Point out each Plasmodium parasite.
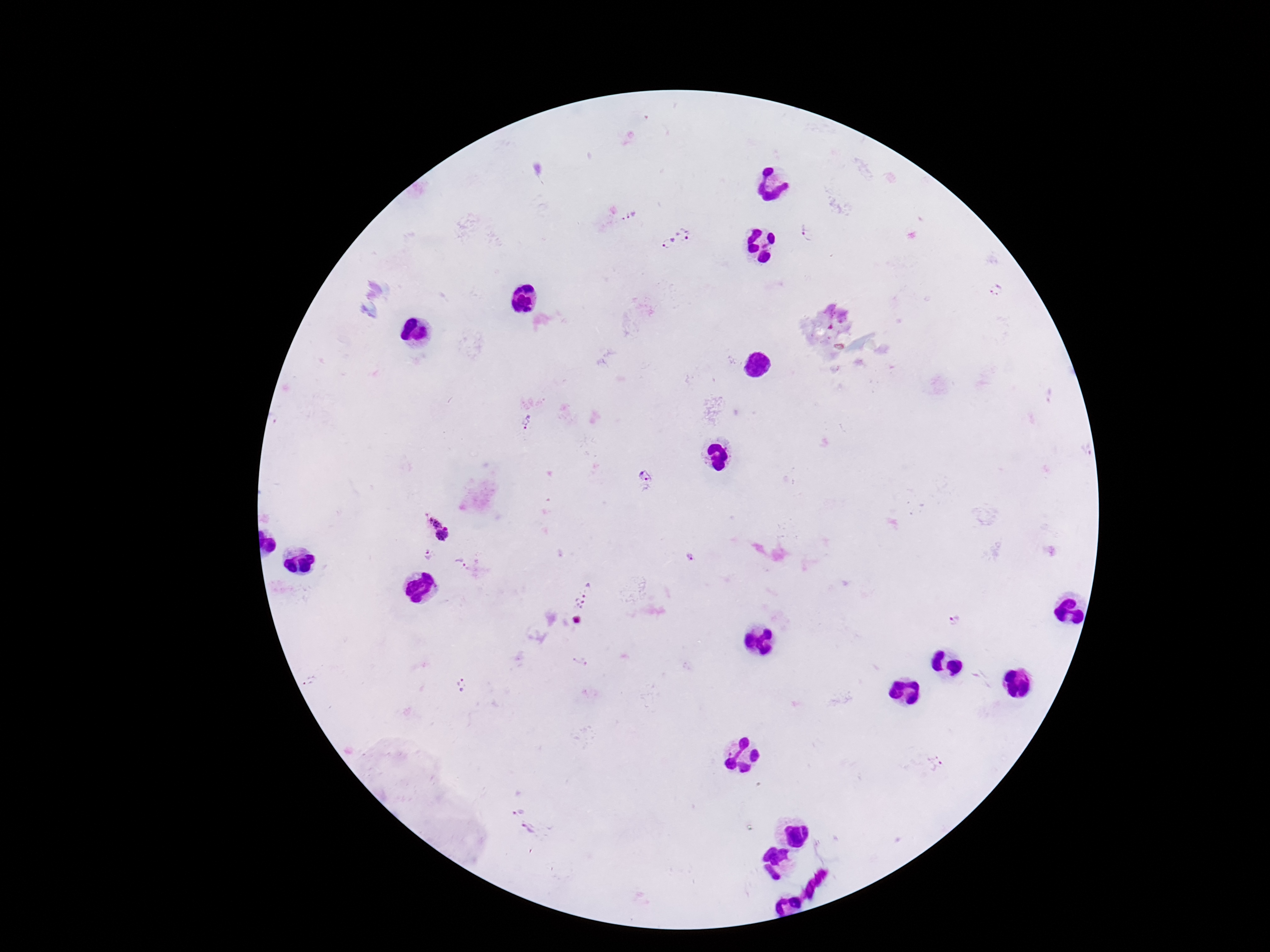
Approximate centers as {x, y} in pixels.
Plasmodium parasites: {632, 217}, {687, 229}, {807, 234}, {668, 243}, {996, 290}, {528, 422}, {646, 473}, {438, 526}, {428, 553}, {461, 562}, {585, 595}, {953, 620}, {935, 762}, {517, 808}, {530, 830}.

Giemsa stain. Patient malaria status: infected. Thick blood smear. Smartphone photograph taken through the microscope eyepiece. 100x magnification. Image is 1270×952 pixels. Single field of view.